Point out each malaria parasite.
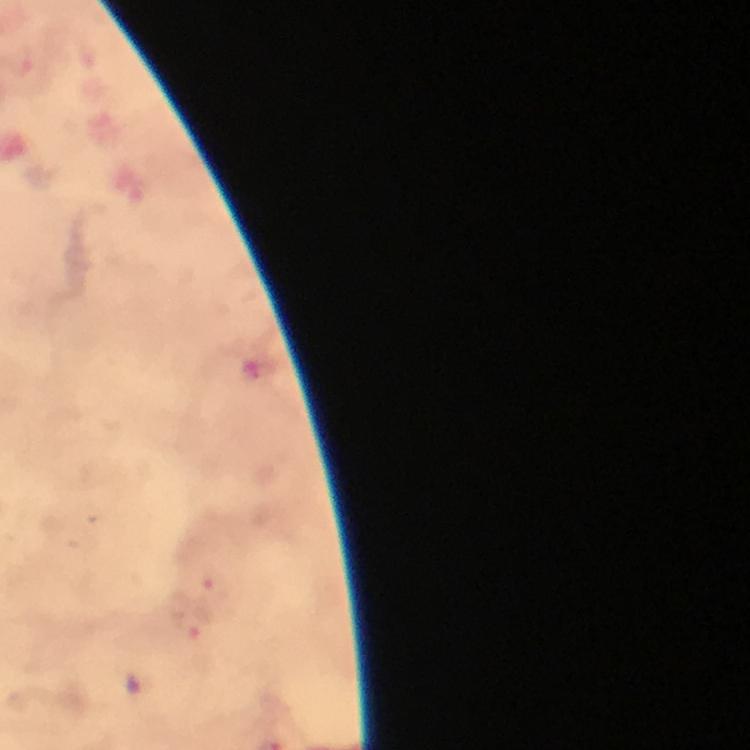
Approximate object centers, in pixels from the top-left corner.
Malaria parasites: (x=210, y=586), (x=188, y=622).

Summary:
  - Magnification: 100x
  - Context: from a malaria diagnostic workup
  - Preparation: thick blood smear
  - Image size: 750×750 pixels
  - Capture: smartphone camera through the microscope
  - Immersion oil: applied
  - Cropped from: a single field of view
  - Stain: Giemsa